Describe the morphology of the erythrocytes.
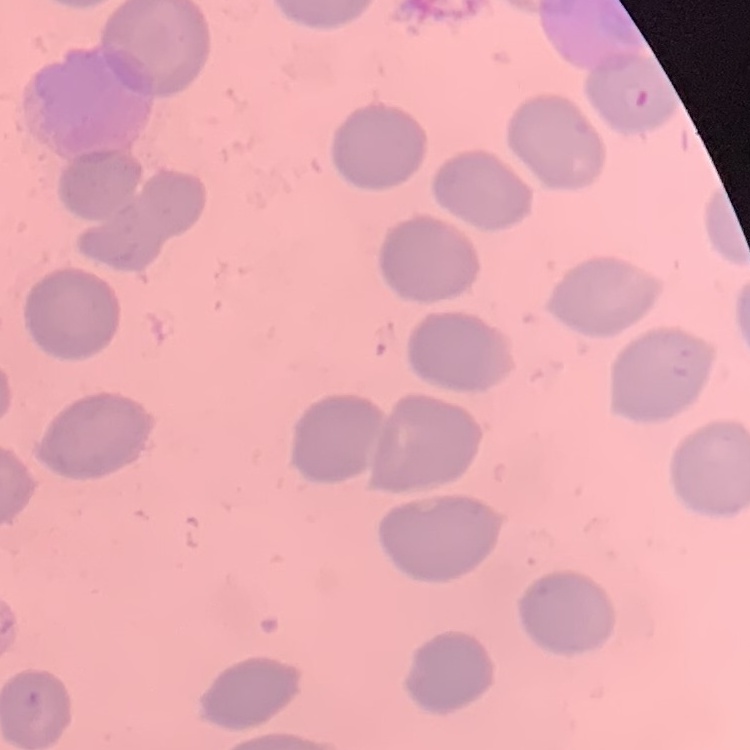

They show no rouleaux formation.

{
  "image_type": "square crop of a larger photomicrograph",
  "stain": "Field's or Giemsa",
  "preparation": "thin blood smear"
}